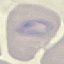
Summary:
  - Malaria status: parasitized
  - Capture: smartphone camera at the microscope eyepiece
  - Image type: cell patch, automatically extracted from a larger field of view and resized to 64 × 64 pixels
  - Stain: Giemsa
  - Preparation: thin blood film